Locate every Plasmodium falciparum-infected red blood cell.
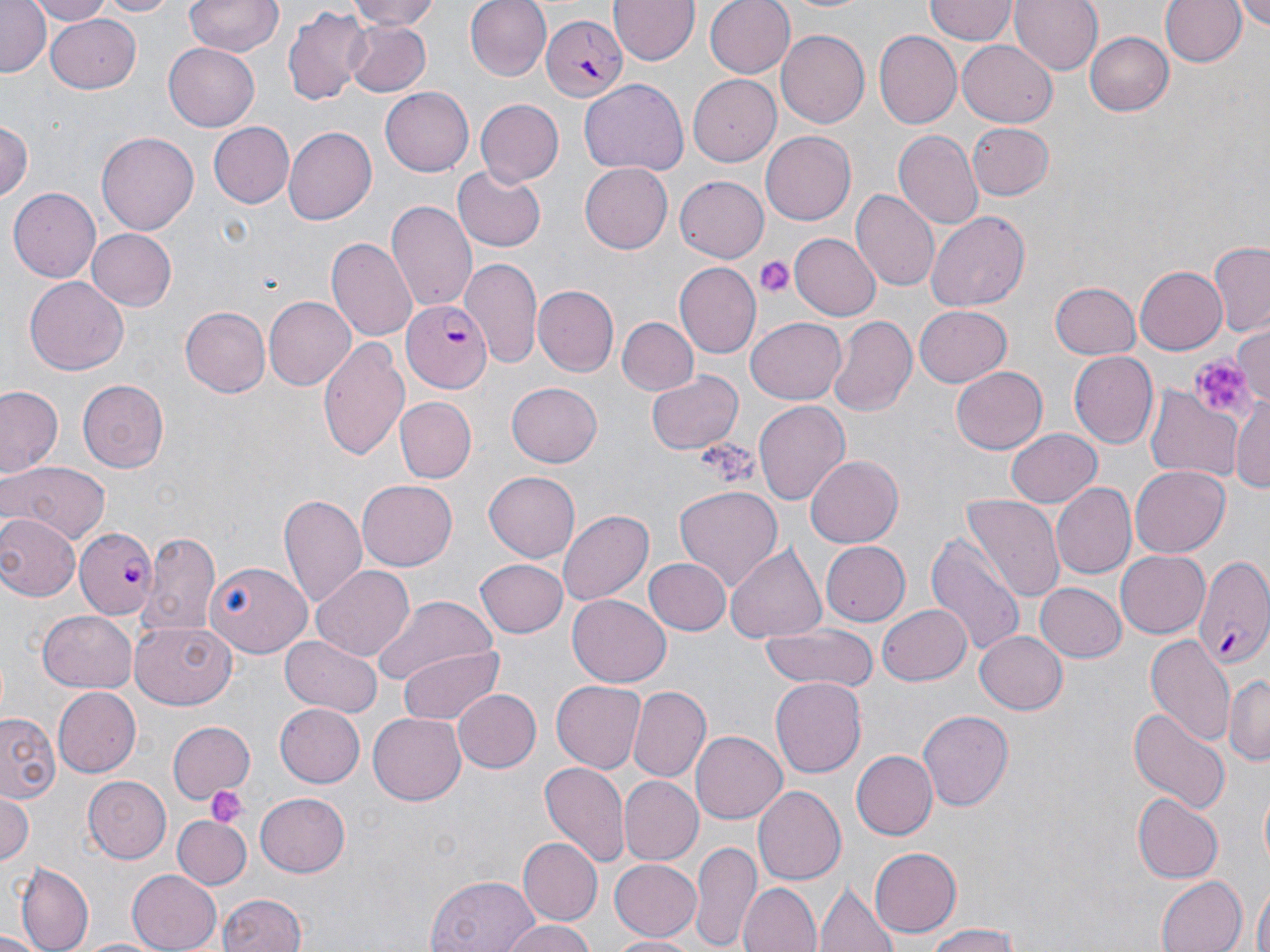
Approximate bounding boxes as named x1/y1/x2/y2 corners in pixels.
Plasmodium falciparum-infected red blood cells: (x1=542, y1=14, x2=627, y2=98), (x1=401, y1=299, x2=491, y2=393), (x1=74, y1=527, x2=159, y2=620), (x1=1195, y1=558, x2=1270, y2=668).

Uninfected red blood cell locations: (x1=0, y1=0, x2=51, y2=77), (x1=32, y1=0, x2=112, y2=25), (x1=92, y1=0, x2=181, y2=18), (x1=184, y1=0, x2=282, y2=57), (x1=343, y1=0, x2=444, y2=29), (x1=466, y1=0, x2=551, y2=81), (x1=610, y1=0, x2=698, y2=65), (x1=705, y1=0, x2=797, y2=77), (x1=782, y1=0, x2=875, y2=15), (x1=926, y1=0, x2=1017, y2=43), (x1=1010, y1=0, x2=1102, y2=76), (x1=1158, y1=0, x2=1243, y2=71), (x1=1232, y1=2, x2=1270, y2=28), (x1=282, y1=4, x2=371, y2=109), (x1=45, y1=12, x2=142, y2=92), (x1=342, y1=19, x2=432, y2=96), (x1=777, y1=30, x2=869, y2=127), (x1=1087, y1=31, x2=1175, y2=116), (x1=874, y1=32, x2=962, y2=128), (x1=958, y1=38, x2=1057, y2=125), (x1=165, y1=43, x2=258, y2=129), (x1=689, y1=74, x2=782, y2=167), (x1=579, y1=79, x2=687, y2=175), (x1=381, y1=85, x2=477, y2=176), (x1=473, y1=99, x2=562, y2=188), (x1=1, y1=115, x2=34, y2=202), (x1=209, y1=122, x2=294, y2=208), (x1=965, y1=122, x2=1057, y2=202), (x1=283, y1=127, x2=377, y2=224), (x1=99, y1=131, x2=198, y2=236), (x1=760, y1=131, x2=856, y2=225), (x1=894, y1=131, x2=983, y2=230), (x1=580, y1=161, x2=673, y2=252), (x1=452, y1=168, x2=546, y2=252), (x1=675, y1=175, x2=769, y2=262), (x1=8, y1=187, x2=101, y2=284), (x1=851, y1=187, x2=939, y2=291), (x1=387, y1=200, x2=476, y2=315), (x1=926, y1=211, x2=1030, y2=311), (x1=87, y1=228, x2=177, y2=312), (x1=789, y1=233, x2=880, y2=320), (x1=328, y1=237, x2=416, y2=340), (x1=1208, y1=244, x2=1269, y2=337), (x1=460, y1=259, x2=543, y2=370), (x1=675, y1=263, x2=760, y2=359), (x1=1136, y1=264, x2=1226, y2=354), (x1=23, y1=276, x2=128, y2=376), (x1=1050, y1=282, x2=1142, y2=360), (x1=534, y1=285, x2=619, y2=376), (x1=262, y1=296, x2=354, y2=391), (x1=180, y1=305, x2=270, y2=397), (x1=915, y1=305, x2=1013, y2=388), (x1=829, y1=316, x2=918, y2=417), (x1=616, y1=317, x2=699, y2=396), (x1=746, y1=317, x2=847, y2=405), (x1=1236, y1=322, x2=1270, y2=399), (x1=318, y1=336, x2=410, y2=458), (x1=1070, y1=351, x2=1158, y2=449), (x1=951, y1=366, x2=1048, y2=455), (x1=645, y1=369, x2=742, y2=456), (x1=77, y1=379, x2=170, y2=472), (x1=505, y1=383, x2=603, y2=467), (x1=0, y1=385, x2=64, y2=480), (x1=1146, y1=386, x2=1244, y2=482), (x1=1232, y1=394, x2=1270, y2=498), (x1=395, y1=397, x2=476, y2=483), (x1=755, y1=400, x2=850, y2=509), (x1=1005, y1=427, x2=1103, y2=508), (x1=802, y1=455, x2=903, y2=549), (x1=0, y1=459, x2=112, y2=546), (x1=1131, y1=465, x2=1230, y2=556), (x1=485, y1=472, x2=579, y2=561), (x1=357, y1=477, x2=456, y2=567), (x1=1052, y1=483, x2=1137, y2=579), (x1=673, y1=486, x2=783, y2=591), (x1=279, y1=492, x2=368, y2=613), (x1=959, y1=495, x2=1065, y2=606), (x1=558, y1=509, x2=653, y2=607), (x1=4, y1=514, x2=76, y2=600), (x1=141, y1=530, x2=221, y2=636), (x1=925, y1=532, x2=1027, y2=662), (x1=818, y1=540, x2=911, y2=627), (x1=726, y1=543, x2=828, y2=645), (x1=1117, y1=549, x2=1210, y2=637), (x1=475, y1=557, x2=568, y2=638), (x1=644, y1=557, x2=731, y2=635), (x1=206, y1=563, x2=311, y2=658), (x1=313, y1=565, x2=416, y2=662), (x1=1037, y1=582, x2=1125, y2=662), (x1=569, y1=593, x2=672, y2=686), (x1=370, y1=596, x2=500, y2=687), (x1=876, y1=603, x2=973, y2=686), (x1=39, y1=607, x2=137, y2=691), (x1=130, y1=621, x2=238, y2=709), (x1=758, y1=622, x2=877, y2=692), (x1=976, y1=630, x2=1069, y2=715), (x1=1144, y1=633, x2=1233, y2=747), (x1=281, y1=636, x2=382, y2=717), (x1=395, y1=644, x2=506, y2=727), (x1=770, y1=675, x2=865, y2=775), (x1=1224, y1=675, x2=1270, y2=765), (x1=550, y1=680, x2=644, y2=773), (x1=628, y1=686, x2=710, y2=783), (x1=52, y1=687, x2=140, y2=777), (x1=454, y1=689, x2=541, y2=772), (x1=276, y1=704, x2=365, y2=787), (x1=1126, y1=705, x2=1230, y2=816), (x1=918, y1=710, x2=1013, y2=810), (x1=369, y1=712, x2=465, y2=806), (x1=1, y1=714, x2=60, y2=803), (x1=167, y1=718, x2=255, y2=804), (x1=691, y1=729, x2=787, y2=820), (x1=851, y1=749, x2=937, y2=839), (x1=537, y1=761, x2=628, y2=869), (x1=618, y1=775, x2=702, y2=865), (x1=86, y1=776, x2=174, y2=863), (x1=753, y1=785, x2=846, y2=887), (x1=0, y1=792, x2=35, y2=866), (x1=254, y1=792, x2=350, y2=876), (x1=1133, y1=795, x2=1224, y2=883), (x1=172, y1=816, x2=250, y2=889), (x1=517, y1=838, x2=601, y2=926), (x1=689, y1=839, x2=763, y2=951), (x1=868, y1=846, x2=962, y2=938), (x1=611, y1=859, x2=701, y2=939), (x1=15, y1=861, x2=93, y2=952), (x1=128, y1=866, x2=224, y2=952), (x1=426, y1=872, x2=544, y2=952), (x1=1154, y1=875, x2=1245, y2=952), (x1=1250, y1=881, x2=1269, y2=952), (x1=739, y1=882, x2=820, y2=952), (x1=816, y1=883, x2=900, y2=952), (x1=218, y1=893, x2=307, y2=952), (x1=497, y1=917, x2=597, y2=952), (x1=922, y1=926, x2=1028, y2=952), (x1=0, y1=931, x2=48, y2=952), (x1=606, y1=933, x2=697, y2=951), (x1=74, y1=936, x2=171, y2=952). Platelet locations: (x1=754, y1=256, x2=794, y2=299), (x1=1185, y1=355, x2=1258, y2=423), (x1=699, y1=438, x2=756, y2=485), (x1=206, y1=789, x2=246, y2=826). Slide-level diagnosis: Plasmodium falciparum. Image is 1270×952 pixels. 1000x magnification. May-Grünwald-Giemsa-stained preparation. Thin blood smear. Optical microscopy. Single field of view.